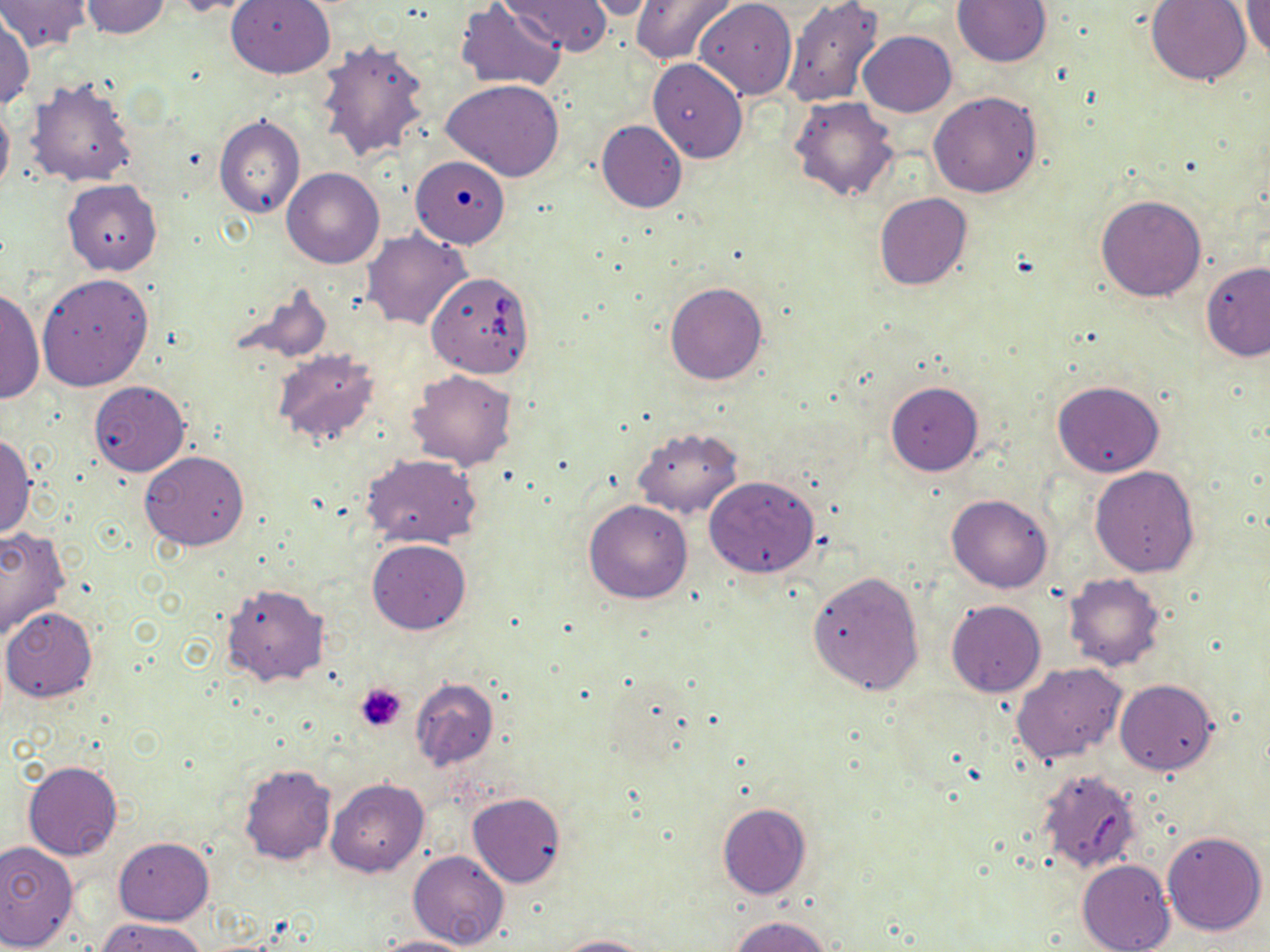

slide-level diagnosis = Babesia divergens
magnification = 1000x
stain = May-Grünwald-Giemsa
image size = 1270×952 pixels
field of view = one of a larger specimen
uninfected red blood cell locations = approximate bounding boxes as [x1, y1, x2, y2] in pixels: [0, 0, 91, 54], [81, 0, 171, 39], [165, 0, 267, 17], [226, 0, 335, 78], [501, 0, 613, 57], [580, 0, 660, 21], [629, 0, 739, 66], [694, 0, 797, 100], [782, 0, 884, 107], [951, 0, 1052, 67], [1146, 0, 1253, 86], [454, 2, 566, 90], [1243, 2, 1270, 63], [0, 15, 34, 110], [858, 31, 957, 116], [315, 40, 431, 164], [648, 58, 748, 163], [26, 78, 138, 187], [441, 79, 566, 183], [928, 91, 1041, 197], [790, 95, 901, 201], [0, 98, 14, 197], [213, 114, 305, 219], [596, 119, 688, 213], [411, 155, 510, 247], [281, 168, 385, 269], [62, 179, 162, 274], [874, 193, 972, 290], [1096, 194, 1206, 302], [363, 229, 473, 330], [1201, 261, 1270, 361], [37, 274, 154, 391], [664, 282, 769, 385], [233, 283, 332, 365], [1, 286, 43, 404], [273, 350, 381, 445], [407, 368, 518, 471], [1051, 379, 1165, 478], [88, 380, 190, 476], [886, 382, 984, 476], [631, 426, 743, 518], [0, 433, 37, 539], [140, 451, 249, 550], [360, 455, 481, 549], [1090, 466, 1200, 576], [704, 475, 819, 577], [946, 493, 1055, 594], [584, 500, 693, 603], [0, 526, 71, 640], [366, 539, 471, 634], [807, 570, 926, 694], [1063, 573, 1166, 672], [221, 583, 330, 687], [946, 600, 1046, 697], [1, 607, 98, 702], [1011, 662, 1130, 763], [411, 678, 500, 770], [1115, 679, 1217, 775], [23, 760, 122, 860], [239, 764, 336, 865], [326, 779, 429, 878], [468, 792, 565, 888], [717, 803, 812, 900], [1162, 829, 1267, 935], [113, 838, 213, 925], [0, 842, 79, 950], [408, 850, 510, 950], [1076, 859, 1175, 952], [729, 915, 837, 952], [95, 917, 209, 952], [550, 934, 650, 952], [372, 936, 476, 952]
Babesia divergens-infected red blood cell locations = approximate bounding boxes as [x1, y1, x2, y2] in pixels: [426, 270, 537, 379]
preparation = thin blood film
modality = light microscopy
platelet locations = approximate bounding boxes as [x1, y1, x2, y2] in pixels: [355, 682, 407, 731]